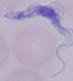
Summary:
  - Modality: micrograph
  - Magnification: 1000x
  - Identification: trypanosome